Report the malaria status.
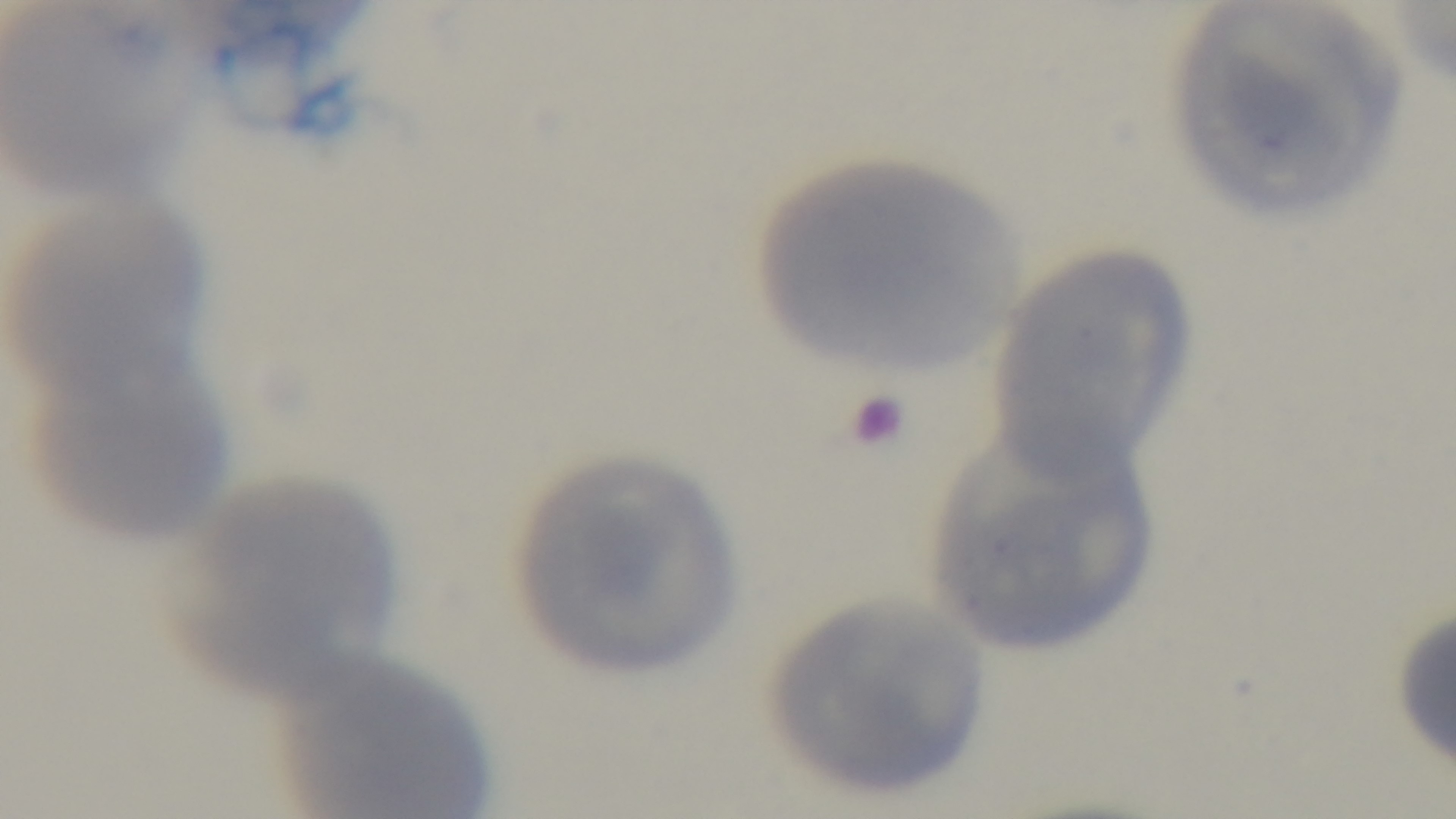
Uninfected.

Summary:
  - Capture: mounted 4K digital camera
  - Objective: 100x oil immersion
  - Field of view: one from the slide
  - Stain: Giemsa
  - Modality: light microscopy
  - Preparation: thin